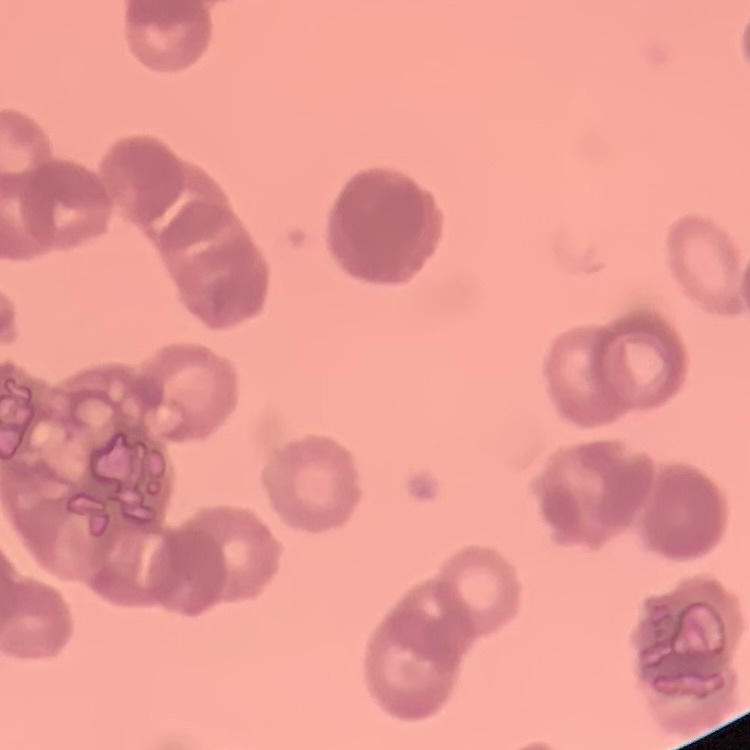
The erythrocytes exhibit rouleaux formation. Thin blood smear. Stained with either Field's or Giemsa. One tile cut from a larger photomicrograph.